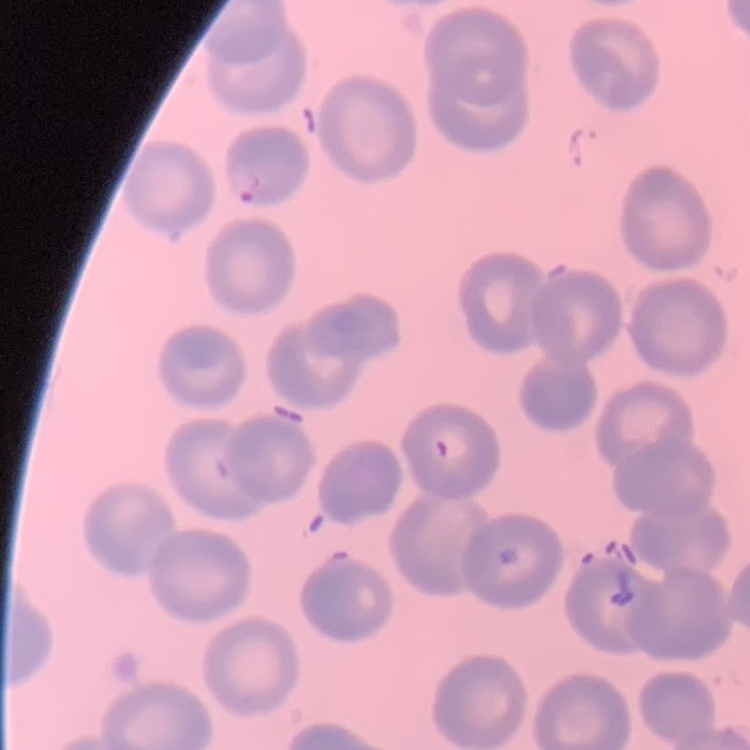
The erythrocytes exhibit no rouleaux formation. Square crop of a larger photomicrograph. Thin blood smear. Field's or Giemsa stain.